Assess this cell for malaria.
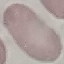

It is uninfected.

Giemsa stain. Photographed with a smartphone camera at the microscope eyepiece. Automatically extracted cell patch, resized to 64 × 64 pixels. Thin smear of blood.